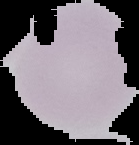

The area outside the segmented cell region is set to black. From a thin blood film. Image is 139×145 pixels. Result: no Plasmodium parasites seen.